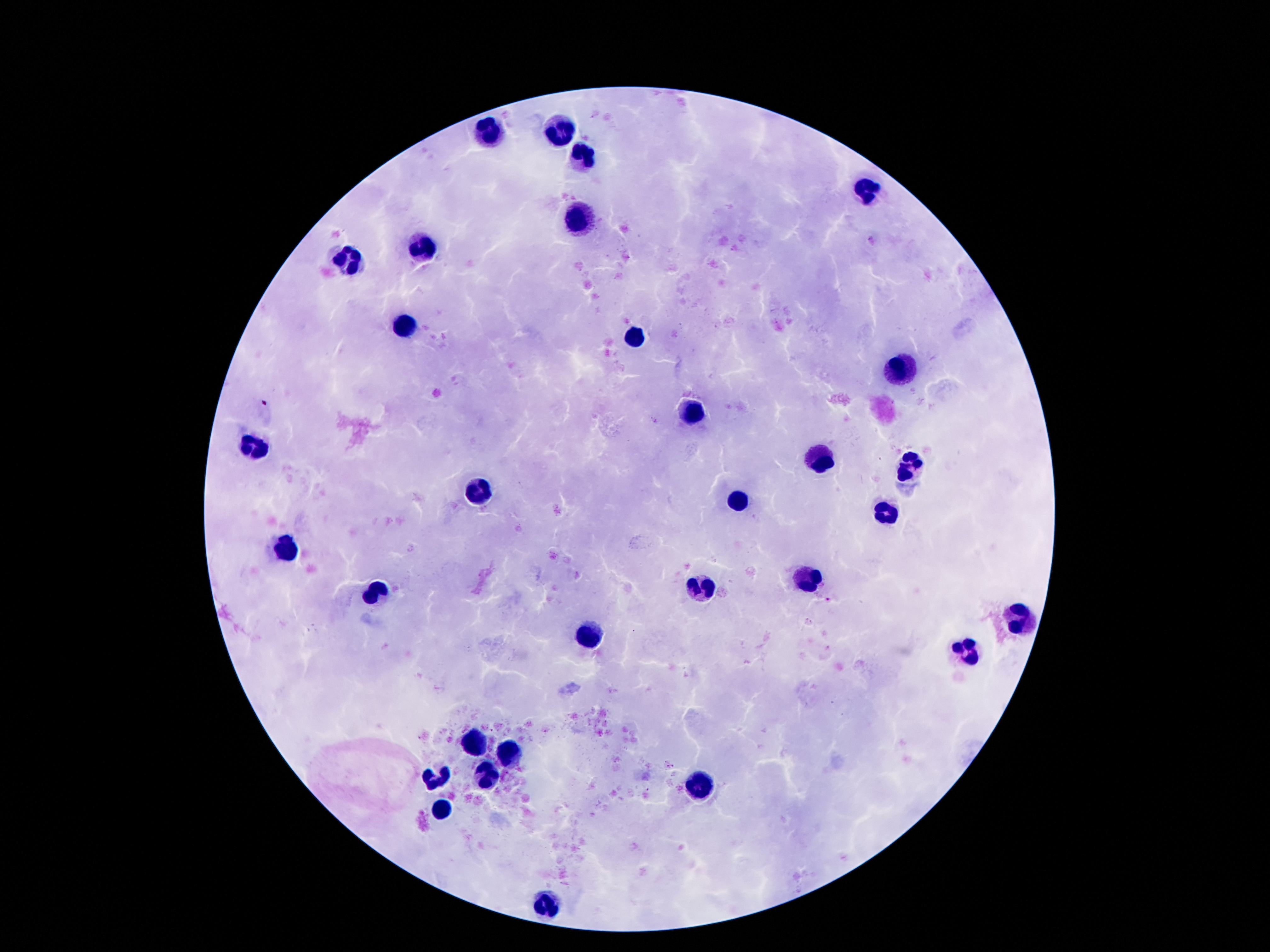

{
  "field_of_view": "single",
  "preparation": "thick blood film",
  "leukocyte_locations": "approximate centers as {x, y} in pixels: {562, 127}, {487, 133}, {581, 156}, {866, 193}, {577, 219}, {418, 245}, {347, 260}, {403, 327}, {631, 338}, {898, 370}, {691, 409}, {252, 439}, {814, 458}, {913, 465}, {480, 492}, {737, 497}, {885, 512}, {284, 550}, {801, 577}, {702, 587}, {375, 592}, {1021, 618}, {588, 634}, {967, 651}, {469, 745}, {510, 757}, {435, 774}, {487, 776}, {702, 787}, {441, 810}, {545, 900}",
  "stain": "Giemsa",
  "magnification": "100x",
  "image_size": "1270×952 pixels",
  "patient_malaria_status": "not infected",
  "capture": "smartphone camera through the microscope eyepiece"
}